Comment on the morphology of the erythrocytes.
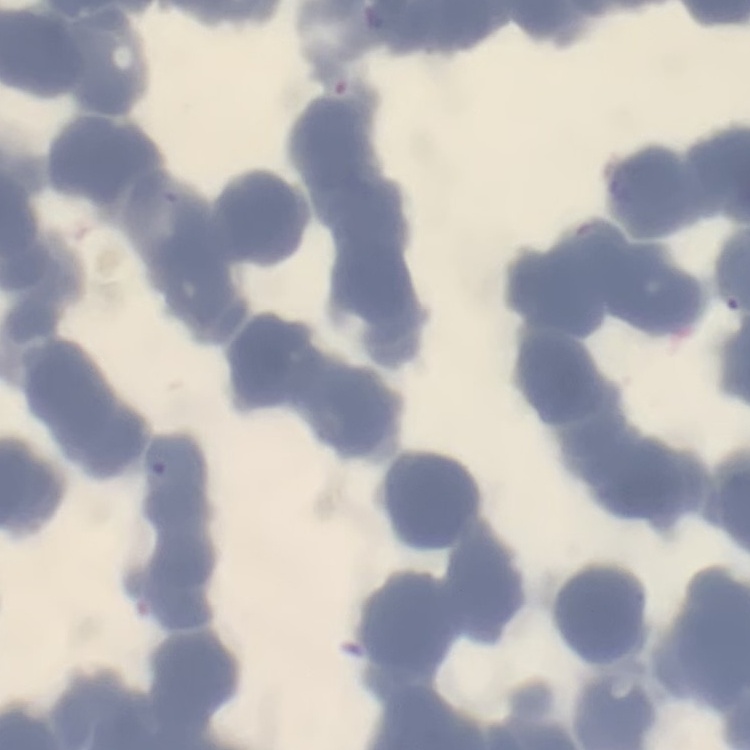

Rouleaux formation.

Thin peripheral smear. One tile cut from a larger photomicrograph. Stained with either Field's or Giemsa.